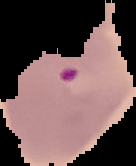
{
  "image_type": "cell region segmented out of the field of view; surrounding area masked to black",
  "malaria_status": "parasitized",
  "image_size": "136×166 pixels",
  "preparation": "thin blood smear"
}